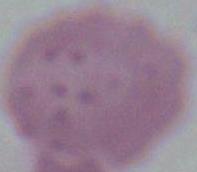 Photomicrograph. A red blood cell is shown. Captured at 1000x magnification.